Describe the morphology of the red blood cells.
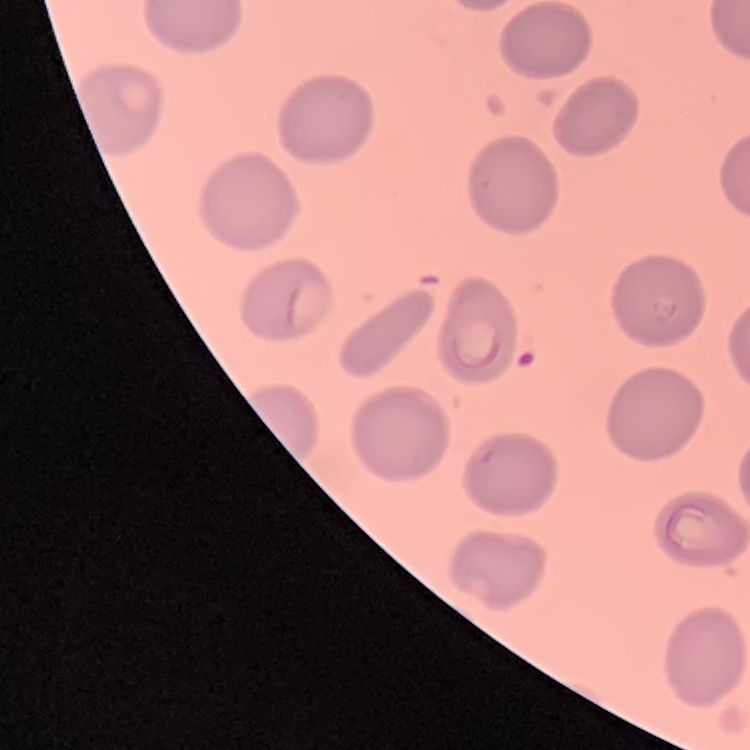
They show no rouleaux formation.

Stained with either Field's or Giemsa. Square crop of a larger photomicrograph. Thin blood film.